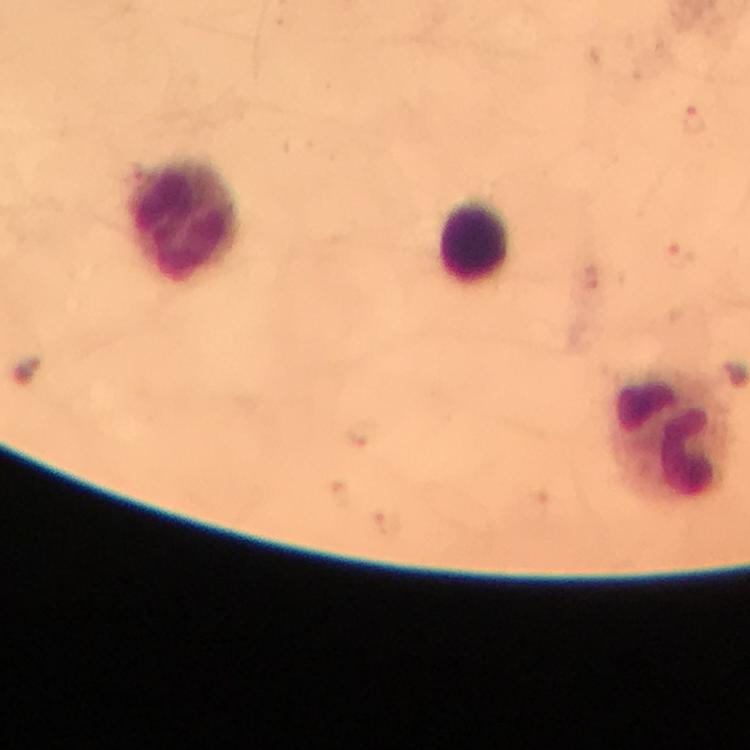
magnification = 100x
immersion oil = applied
stain = Giemsa
cropped from = one field of view
image size = 750×750 pixels
malaria parasite locations = approximate centers as {x, y} in pixels: {694, 119}, {681, 254}
leukocyte locations = approximate centers as {x, y} in pixels: {184, 220}, {473, 242}, {671, 439}
capture = smartphone photograph through a microscope
preparation = thick blood film
context = from a diagnostic examination for malaria